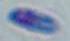

Summary:
  - Modality: photomicrograph
  - Magnification: 1000x
  - Identification: Toxoplasma gondii